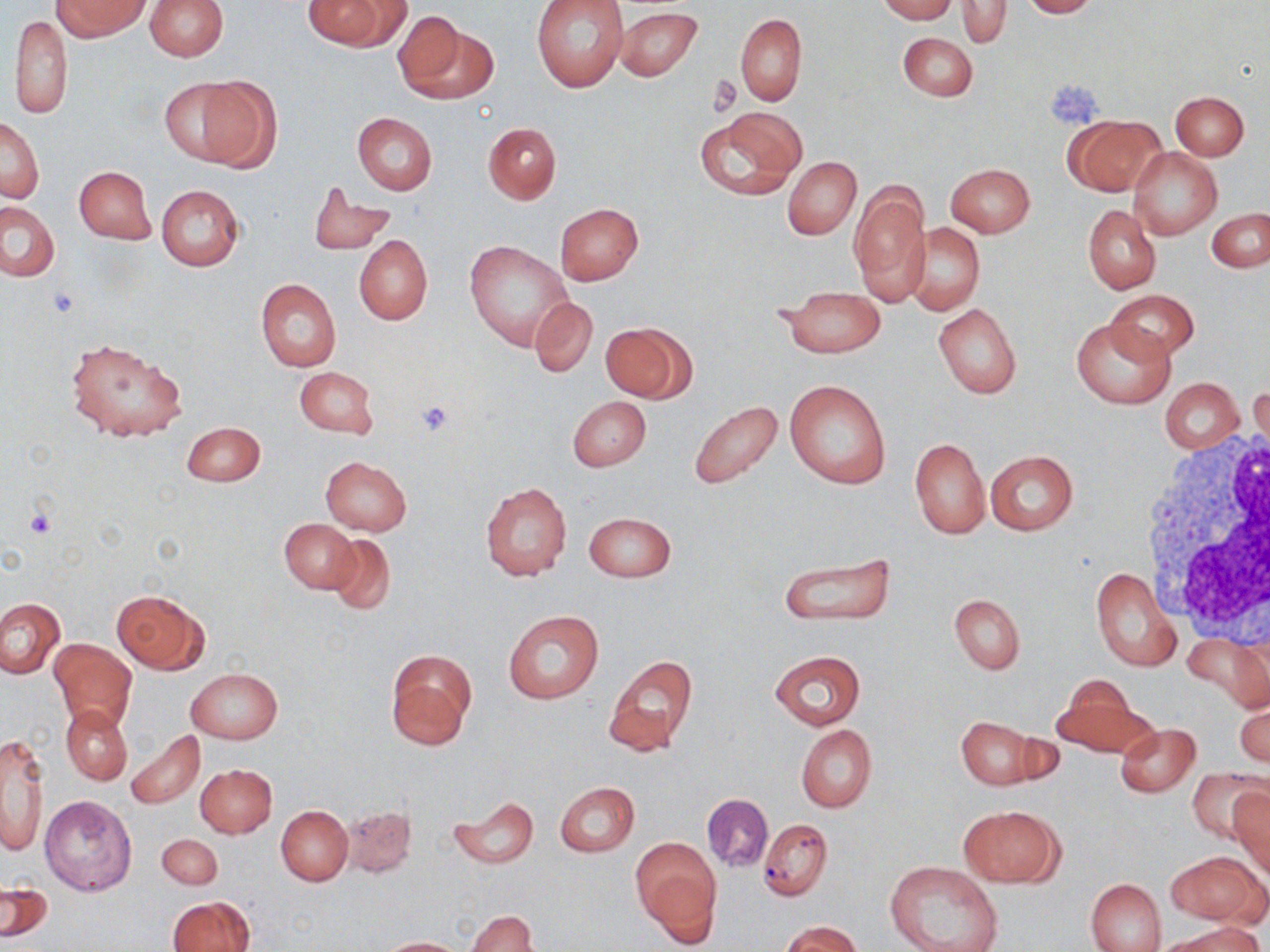
slide-level diagnosis = negative for blood parasites
magnification = 1000x
modality = light microscopy
platelet locations = approximate bounding boxes as named x1/y1/x2/y2 corners in pixels: (x1=709, y1=75, x2=740, y2=117), (x1=1048, y1=80, x2=1104, y2=126), (x1=413, y1=400, x2=456, y2=438), (x1=25, y1=507, x2=57, y2=539)
stain = May-Grünwald-Giemsa
uninfected red blood cell locations = approximate bounding boxes as named x1/y1/x2/y2 corners in pixels: (x1=53, y1=0, x2=149, y2=40), (x1=146, y1=0, x2=227, y2=60), (x1=304, y1=0, x2=407, y2=52), (x1=531, y1=0, x2=628, y2=92), (x1=878, y1=0, x2=955, y2=22), (x1=956, y1=0, x2=1012, y2=48), (x1=1020, y1=0, x2=1098, y2=18), (x1=615, y1=7, x2=702, y2=84), (x1=390, y1=9, x2=485, y2=103), (x1=8, y1=11, x2=72, y2=120), (x1=734, y1=12, x2=807, y2=105), (x1=898, y1=32, x2=978, y2=101), (x1=178, y1=75, x2=280, y2=172), (x1=1170, y1=91, x2=1248, y2=159), (x1=694, y1=109, x2=806, y2=201), (x1=351, y1=113, x2=437, y2=195), (x1=1064, y1=115, x2=1164, y2=197), (x1=1, y1=118, x2=44, y2=203), (x1=482, y1=121, x2=562, y2=204), (x1=1129, y1=148, x2=1221, y2=240), (x1=783, y1=156, x2=861, y2=239), (x1=946, y1=163, x2=1035, y2=238), (x1=74, y1=166, x2=155, y2=244), (x1=849, y1=179, x2=931, y2=308), (x1=156, y1=184, x2=244, y2=270), (x1=308, y1=185, x2=396, y2=254), (x1=1, y1=202, x2=60, y2=281), (x1=555, y1=203, x2=643, y2=285), (x1=1083, y1=205, x2=1161, y2=294), (x1=1207, y1=209, x2=1270, y2=272), (x1=907, y1=224, x2=985, y2=316), (x1=354, y1=235, x2=433, y2=326), (x1=464, y1=240, x2=572, y2=350), (x1=255, y1=278, x2=341, y2=372), (x1=777, y1=287, x2=887, y2=358), (x1=1103, y1=289, x2=1200, y2=361), (x1=530, y1=296, x2=597, y2=378), (x1=933, y1=304, x2=1022, y2=397), (x1=1071, y1=316, x2=1174, y2=408), (x1=601, y1=322, x2=693, y2=403), (x1=65, y1=336, x2=187, y2=442), (x1=294, y1=365, x2=379, y2=440), (x1=1161, y1=378, x2=1244, y2=454), (x1=784, y1=379, x2=891, y2=490), (x1=1250, y1=381, x2=1269, y2=464), (x1=567, y1=396, x2=650, y2=472), (x1=688, y1=401, x2=785, y2=490), (x1=182, y1=422, x2=265, y2=487), (x1=909, y1=437, x2=989, y2=539), (x1=985, y1=450, x2=1078, y2=535), (x1=320, y1=457, x2=412, y2=536), (x1=480, y1=483, x2=572, y2=582), (x1=584, y1=512, x2=676, y2=582), (x1=280, y1=519, x2=359, y2=594), (x1=325, y1=531, x2=397, y2=617), (x1=780, y1=552, x2=895, y2=627), (x1=1089, y1=567, x2=1181, y2=672), (x1=111, y1=590, x2=208, y2=674), (x1=949, y1=594, x2=1025, y2=675), (x1=0, y1=598, x2=66, y2=679), (x1=502, y1=610, x2=602, y2=705), (x1=1185, y1=633, x2=1269, y2=711), (x1=49, y1=638, x2=137, y2=733), (x1=384, y1=649, x2=476, y2=749), (x1=769, y1=650, x2=866, y2=730), (x1=604, y1=654, x2=698, y2=757), (x1=187, y1=667, x2=282, y2=744), (x1=1050, y1=679, x2=1154, y2=760), (x1=1235, y1=700, x2=1269, y2=771), (x1=61, y1=705, x2=133, y2=786), (x1=955, y1=715, x2=1049, y2=790), (x1=1115, y1=722, x2=1200, y2=797), (x1=795, y1=725, x2=877, y2=812), (x1=124, y1=730, x2=204, y2=810), (x1=1, y1=736, x2=49, y2=859), (x1=195, y1=765, x2=277, y2=838), (x1=1188, y1=768, x2=1268, y2=847), (x1=554, y1=782, x2=640, y2=857), (x1=1228, y1=790, x2=1270, y2=876), (x1=702, y1=793, x2=773, y2=872), (x1=40, y1=795, x2=137, y2=895), (x1=448, y1=795, x2=539, y2=869), (x1=341, y1=804, x2=417, y2=878), (x1=955, y1=804, x2=1065, y2=888), (x1=276, y1=807, x2=352, y2=885), (x1=759, y1=818, x2=833, y2=901), (x1=157, y1=834, x2=222, y2=889), (x1=631, y1=837, x2=721, y2=941), (x1=1166, y1=851, x2=1264, y2=926), (x1=884, y1=861, x2=1004, y2=952), (x1=1085, y1=877, x2=1166, y2=952), (x1=2, y1=881, x2=53, y2=943), (x1=168, y1=896, x2=255, y2=952), (x1=468, y1=910, x2=538, y2=952), (x1=783, y1=921, x2=862, y2=952), (x1=1168, y1=922, x2=1263, y2=952), (x1=376, y1=937, x2=469, y2=951)
preparation = thin blood film
field of view = single
image size = 1270×952 pixels
white blood cell locations = approximate bounding boxes as named x1/y1/x2/y2 corners in pixels: (x1=1140, y1=425, x2=1270, y2=635)